Describe the morphology of the erythrocytes.
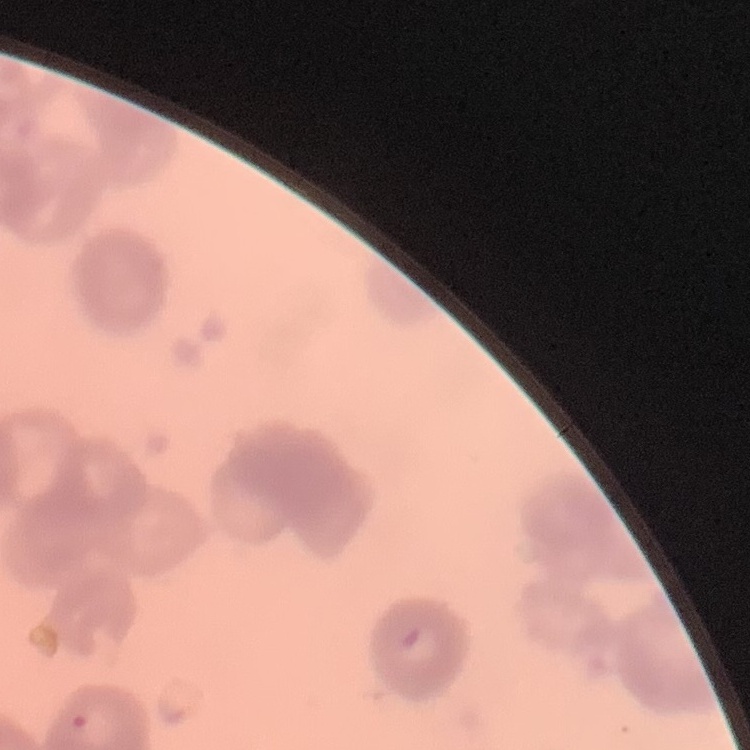

Rouleaux formation.

Field's or Giemsa stain. Thin peripheral smear. One tile cut from a larger photomicrograph.